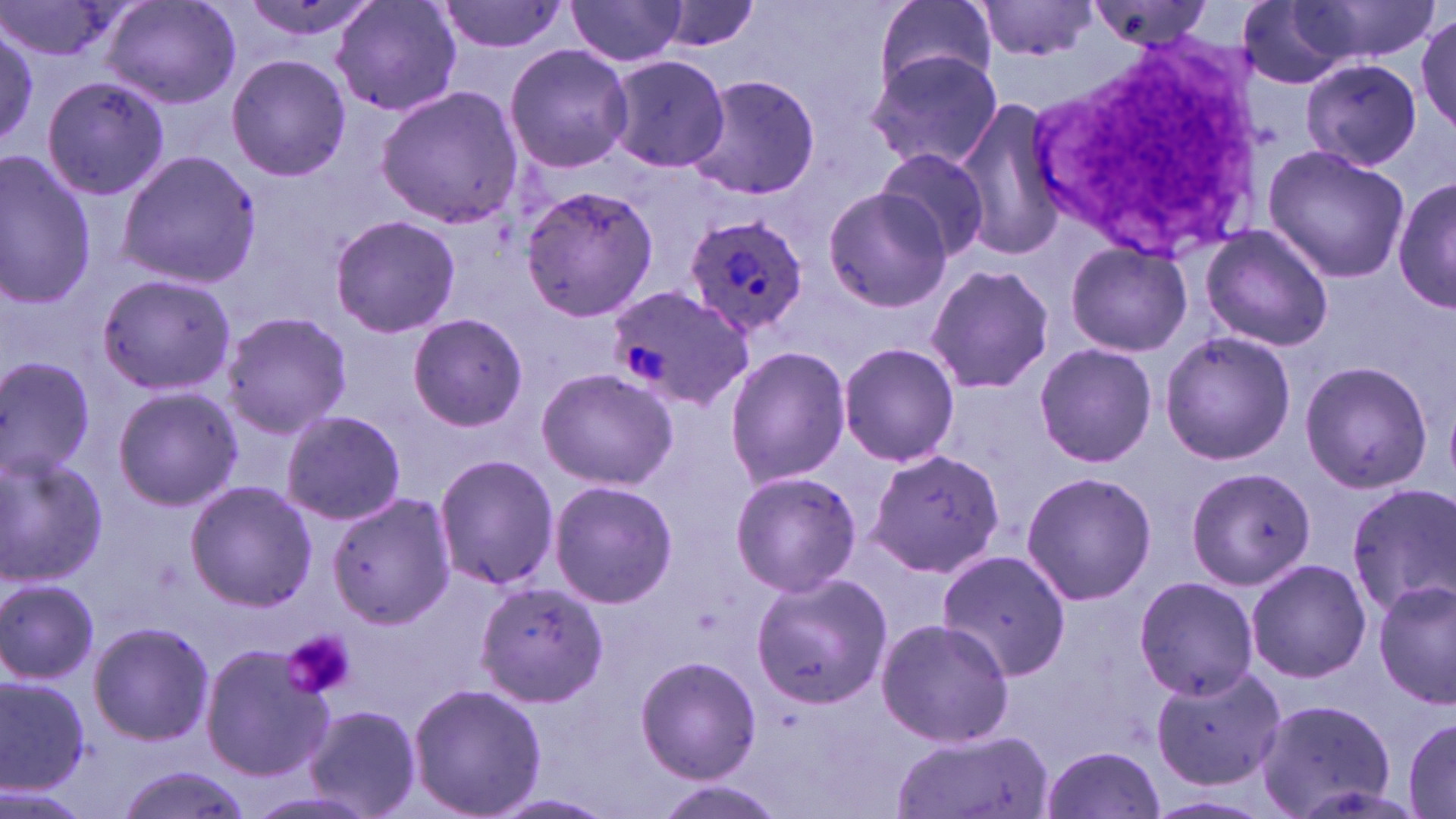
Summary:
  - Coordinate format: approximate bounding boxes as [x1, y1, x2, y2] in pixels
  - Plasmodium ovale-infected red blood cell locations: [683, 214, 809, 339], [610, 285, 754, 411]
  - White blood cell locations: [1026, 32, 1274, 254]
  - Platelet locations: [280, 628, 356, 700]
  - Uninfected red blood cell locations: [0, 0, 121, 66], [103, 0, 239, 108], [331, 0, 463, 118], [437, 0, 570, 55], [876, 0, 999, 93], [1301, 0, 1438, 63], [239, 1, 380, 46], [563, 1, 691, 67], [974, 1, 1098, 59], [1082, 1, 1221, 50], [1236, 1, 1358, 89], [652, 2, 764, 53], [1416, 12, 1454, 133], [1, 22, 40, 153], [503, 43, 634, 173], [864, 49, 1004, 172], [608, 53, 731, 173], [225, 55, 351, 180], [1301, 58, 1423, 170], [41, 75, 170, 202], [685, 75, 824, 202], [375, 86, 523, 228], [949, 99, 1070, 262], [1262, 145, 1410, 283], [874, 148, 991, 262], [0, 150, 98, 310], [117, 151, 262, 286], [1392, 171, 1455, 317], [519, 183, 660, 321], [821, 186, 953, 312], [329, 213, 462, 339], [1199, 224, 1334, 353], [1061, 238, 1196, 357], [925, 264, 1056, 395], [96, 272, 236, 396], [218, 312, 355, 439], [407, 314, 528, 431], [1159, 330, 1296, 466], [836, 341, 961, 467], [1033, 343, 1158, 468], [723, 346, 850, 488], [0, 358, 97, 480], [1299, 359, 1433, 495], [535, 368, 679, 492], [113, 385, 242, 512], [281, 409, 406, 525], [866, 448, 1006, 576], [1, 451, 110, 585], [434, 454, 558, 591], [1185, 467, 1317, 590], [728, 469, 861, 598], [1021, 470, 1157, 606], [549, 479, 677, 609], [184, 480, 317, 611], [1347, 483, 1456, 614], [328, 493, 452, 630], [938, 547, 1073, 682], [1244, 558, 1372, 683], [749, 573, 892, 708], [1135, 574, 1260, 699], [0, 577, 100, 683], [1374, 577, 1454, 708], [474, 582, 609, 708], [875, 617, 1017, 749], [87, 622, 215, 746], [199, 642, 334, 781], [634, 655, 761, 784], [1149, 663, 1287, 791], [0, 671, 91, 795], [407, 682, 547, 818], [1254, 697, 1396, 819], [304, 703, 421, 818], [1401, 714, 1456, 819], [887, 729, 1050, 819], [1038, 744, 1166, 819], [114, 764, 258, 819], [650, 779, 782, 819], [489, 793, 618, 818]
  - Slide-level diagnosis: Plasmodium ovale
  - Preparation: thin blood film
  - Image size: 1456×819 pixels
  - Modality: optical microscopy
  - Stain: May-Grünwald-Giemsa
  - Field of view: single
  - Magnification: 1000x